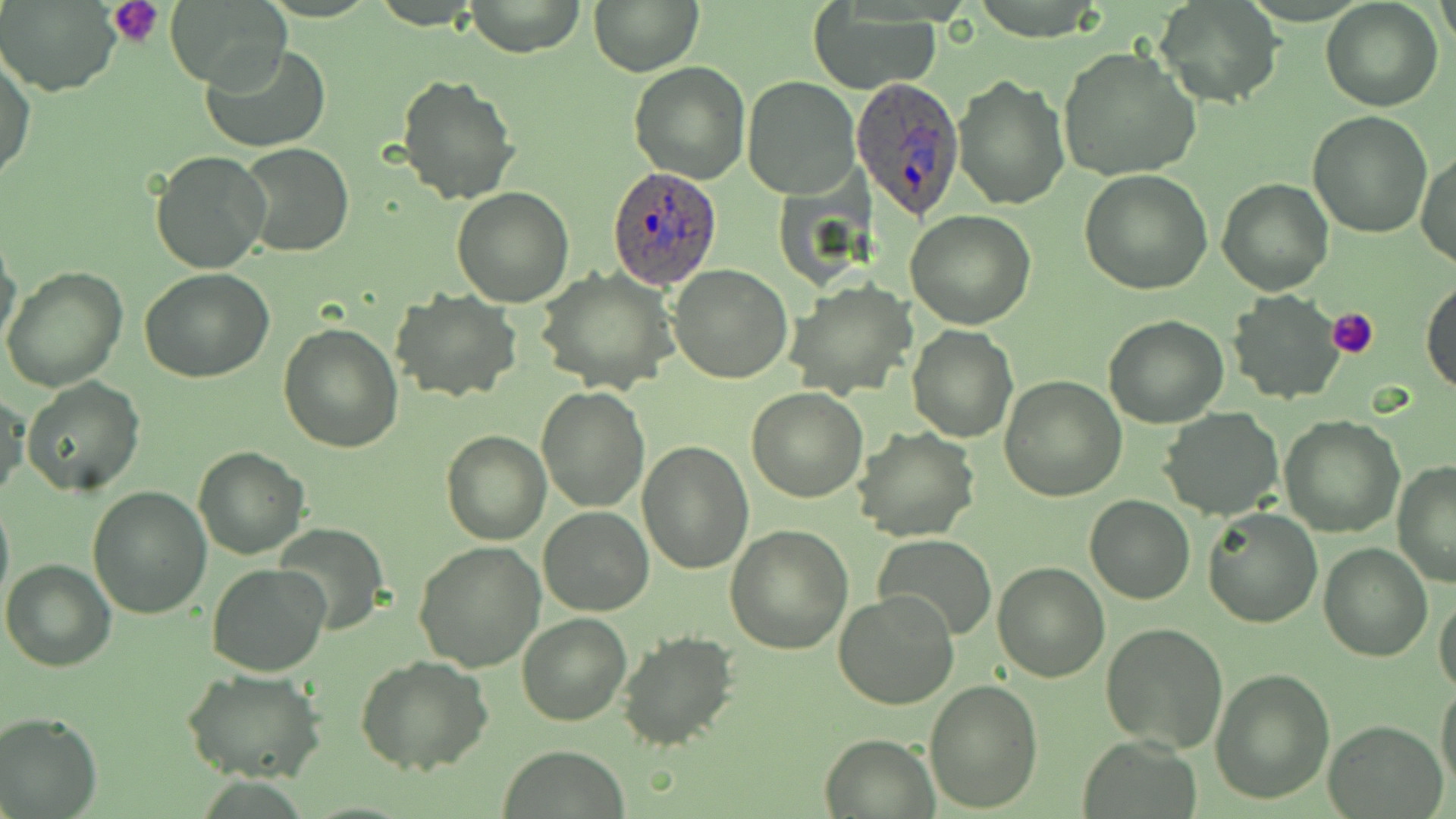

slide-level diagnosis = Plasmodium ovale
preparation = thin blood film
Plasmodium ovale-infected red blood cell locations = approximate bounding boxes as [x1, y1, x2, y2] in pixels: [849, 74, 966, 222], [609, 166, 723, 290]
uninfected red blood cell locations = approximate bounding boxes as [x1, y1, x2, y2] in pixels: [163, 0, 293, 92], [465, 0, 585, 57], [1156, 0, 1281, 105], [1436, 0, 1455, 53], [1, 1, 121, 97], [591, 1, 700, 75], [1320, 1, 1444, 112], [808, 9, 943, 93], [203, 43, 330, 151], [1058, 46, 1201, 181], [1, 50, 36, 185], [628, 61, 750, 185], [396, 74, 522, 207], [953, 74, 1069, 211], [742, 77, 860, 199], [1306, 111, 1434, 239], [237, 143, 355, 259], [1416, 149, 1455, 271], [150, 151, 273, 275], [1081, 170, 1212, 295], [1216, 178, 1332, 296], [451, 187, 573, 306], [905, 210, 1037, 330], [0, 234, 22, 356], [670, 263, 792, 383], [2, 267, 127, 392], [141, 269, 275, 382], [537, 269, 676, 395], [1420, 276, 1456, 395], [786, 282, 916, 399], [392, 290, 521, 403], [1227, 291, 1346, 405], [1103, 314, 1228, 428], [278, 321, 404, 452], [907, 325, 1018, 442], [999, 376, 1126, 501], [22, 377, 144, 495], [535, 387, 650, 513], [747, 387, 868, 503], [0, 391, 28, 505], [1160, 408, 1283, 521], [1279, 414, 1404, 537], [854, 427, 980, 542], [441, 429, 551, 546], [638, 440, 754, 575], [192, 447, 309, 560], [1393, 460, 1456, 589], [88, 484, 211, 619], [0, 494, 13, 614], [1085, 495, 1194, 604], [539, 505, 653, 615], [1203, 507, 1323, 628], [275, 523, 388, 635], [725, 523, 853, 655], [876, 535, 997, 640], [413, 539, 545, 672], [1319, 542, 1431, 661], [2, 559, 117, 671], [991, 560, 1109, 682], [207, 563, 329, 677], [833, 590, 961, 711], [1433, 590, 1456, 696], [517, 613, 632, 727], [1100, 622, 1228, 752], [617, 630, 738, 752], [355, 654, 493, 776], [1209, 668, 1334, 804], [181, 669, 327, 783], [924, 677, 1043, 812], [1436, 679, 1456, 794], [0, 711, 101, 818], [1323, 719, 1448, 817], [818, 734, 940, 817], [1080, 739, 1200, 819], [499, 747, 629, 818]
modality = light microscopy
field of view = one of a larger specimen
platelet locations = approximate bounding boxes as [x1, y1, x2, y2] in pixels: [108, 0, 166, 47], [1327, 306, 1379, 360]
image size = 1456×819 pixels
stain = May-Grünwald-Giemsa
magnification = 1000x